Locate platelets.
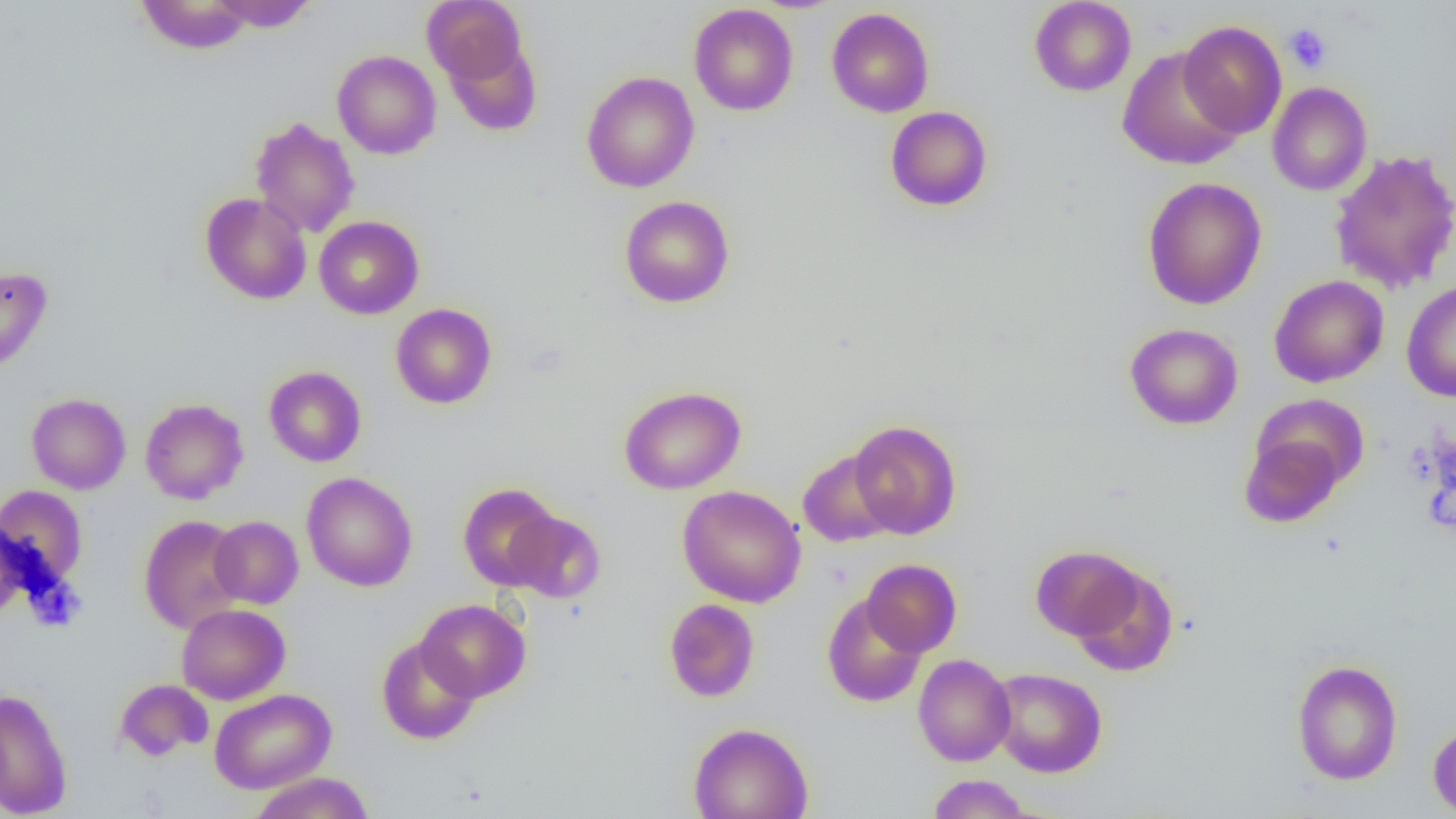
Approximate bounding boxes as [x1, y1, x2, y2] in pixels.
Platelets: [1283, 23, 1333, 74].

Uninfected red blood cell locations: [135, 0, 254, 54], [209, 0, 319, 32], [422, 0, 527, 87], [1029, 0, 1136, 97], [689, 3, 798, 116], [826, 7, 934, 117], [1178, 20, 1287, 138], [1117, 48, 1245, 170], [332, 50, 441, 159], [581, 71, 699, 193], [1267, 81, 1372, 196], [885, 106, 993, 211], [249, 116, 360, 238], [1329, 149, 1456, 294], [1141, 177, 1267, 309], [199, 192, 312, 305], [619, 195, 735, 308], [314, 216, 424, 319], [0, 266, 53, 373], [1269, 275, 1389, 388], [1401, 280, 1456, 402], [390, 303, 497, 409], [1124, 323, 1243, 430], [264, 365, 367, 467], [619, 385, 746, 495], [26, 393, 131, 495], [140, 398, 249, 504], [848, 419, 962, 539], [1239, 432, 1347, 528], [798, 449, 898, 547], [302, 472, 418, 591], [457, 483, 561, 590], [0, 485, 88, 587], [677, 485, 807, 608], [505, 509, 606, 603], [138, 514, 247, 633], [209, 516, 303, 609], [1030, 545, 1144, 642], [861, 559, 962, 657], [1068, 564, 1178, 677], [821, 594, 927, 707], [663, 598, 760, 702], [415, 599, 531, 702], [176, 603, 290, 704], [376, 636, 481, 745], [913, 654, 1016, 766], [1290, 659, 1403, 785], [988, 667, 1108, 777], [114, 678, 213, 762], [0, 687, 73, 818], [209, 688, 336, 794], [1427, 721, 1456, 817], [687, 722, 813, 819], [248, 772, 375, 819], [926, 774, 1033, 818]. Slide-level diagnosis: negative for blood parasites. Image is 1456×819 pixels. Captured at 1000x magnification. Optical microscopy. One field of a larger specimen. Thin blood film.